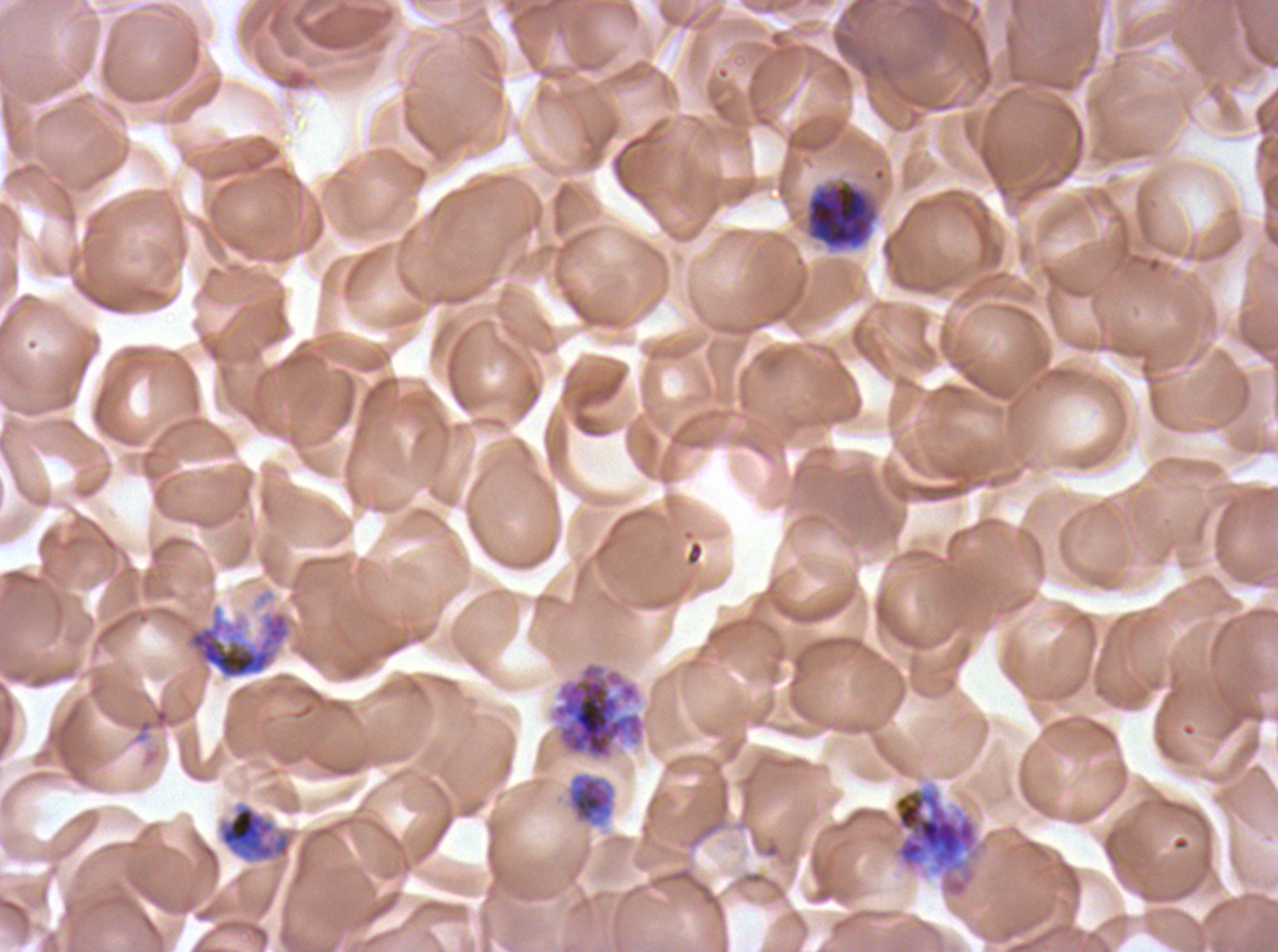
Approximate bounding rectangles given as corner coordinates in pixels from the top-left. Late trophozoite locations: (x1=217, y1=802, x2=292, y2=863). Early schizont locations: (x1=805, y1=181, x2=878, y2=250), (x1=186, y1=608, x2=291, y2=679), (x1=892, y1=785, x2=981, y2=898). Segmenter locations: (x1=547, y1=659, x2=649, y2=763). Mid trophozoite locations: (x1=567, y1=773, x2=615, y2=824). Giemsa stain. One sub-image of a larger composite. P. falciparum from a patient in The Gambia, cultured ex vivo for 24 to 48 hours. Image is 1278×952 pixels. Thin blood film. Life-cycle stages observed: mid trophozoite, late trophozoite, early schizont, segmenter.